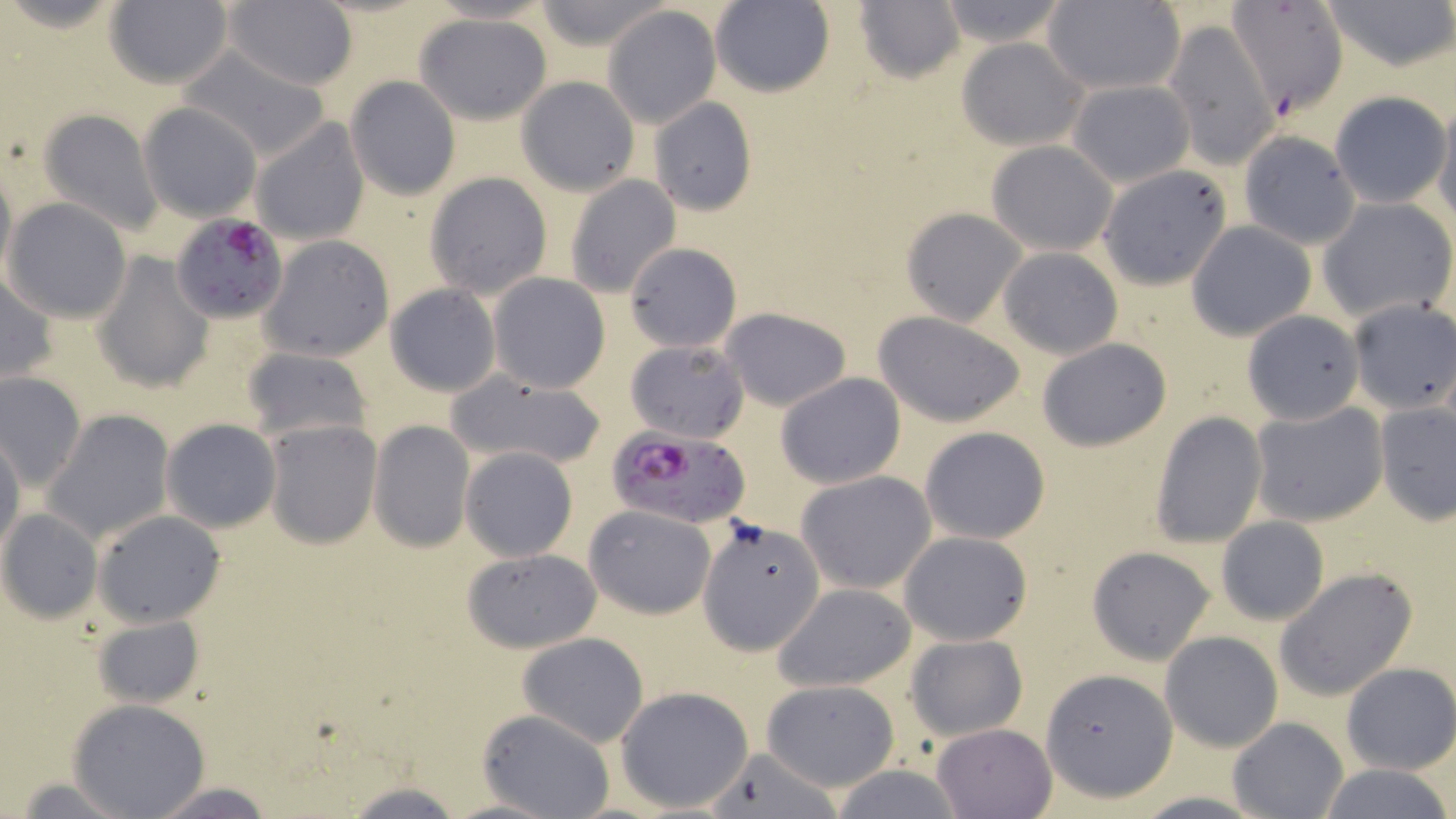
Summary:
  - Coordinate format: approximate bounding boxes as (x1,y1)-(x2,y2) corner pairs in pixels
  - Plasmodium falciparum-infected red blood cell locations: (171,212)-(290,325), (612,425)-(747,527)
  - Uninfected red blood cell locations: (105,0)-(233,89), (221,0)-(358,90), (530,0)-(674,50), (934,0)-(1071,48), (1316,0)-(1456,75), (710,1)-(836,97), (852,1)-(967,84), (1224,1)-(1350,115), (1043,2)-(1185,94), (603,7)-(720,128), (414,13)-(553,123), (1162,19)-(1278,170), (956,37)-(1087,151), (179,48)-(332,161), (345,76)-(460,201), (515,77)-(639,197), (1067,79)-(1195,187), (1330,92)-(1450,208), (648,96)-(757,215), (1432,97)-(1456,227), (138,102)-(264,221), (38,108)-(162,233), (250,116)-(371,246), (1236,130)-(1361,248), (986,139)-(1119,255), (0,162)-(16,291), (1100,164)-(1232,287), (425,172)-(554,299), (563,175)-(681,300), (4,197)-(133,323), (1318,197)-(1455,321), (902,207)-(1026,326), (1187,221)-(1316,340), (259,235)-(395,363), (625,242)-(743,352), (998,246)-(1123,359), (93,251)-(214,392), (1,273)-(58,384), (488,273)-(610,393), (385,282)-(501,397), (1346,300)-(1456,414), (720,307)-(852,410), (1243,309)-(1364,427), (871,310)-(1028,426), (1036,338)-(1173,451), (624,339)-(750,444), (241,347)-(372,443), (446,370)-(608,470), (0,371)-(86,489), (777,372)-(905,489), (1248,399)-(1389,527), (1374,401)-(1456,525), (42,409)-(175,546), (1151,414)-(1268,547), (162,418)-(281,534), (263,419)-(382,549), (368,420)-(475,552), (920,426)-(1050,544), (0,434)-(24,558), (460,447)-(578,561), (796,471)-(935,595), (584,503)-(717,618), (0,509)-(103,623), (94,510)-(227,628), (1215,516)-(1329,626), (699,518)-(826,655), (899,531)-(1032,644), (1087,545)-(1215,665), (461,548)-(603,653), (1274,567)-(1419,703), (771,581)-(918,692), (91,615)-(205,708), (1160,631)-(1283,751), (517,632)-(650,747), (905,634)-(1027,740), (1341,663)-(1456,776), (1041,669)-(1178,801), (759,680)-(900,791), (615,685)-(755,814), (67,698)-(212,819), (476,708)-(618,819), (1227,717)-(1347,819), (931,723)-(1056,818), (702,745)-(844,819), (1313,763)-(1456,819), (7,774)-(143,817), (339,779)-(468,818), (147,781)-(279,818)
  - Slide-level diagnosis: Plasmodium falciparum
  - Stain: May-Grünwald-Giemsa
  - Magnification: 1000x
  - Modality: optical microscopy
  - Preparation: thin blood smear
  - Field of view: one of a larger specimen
  - Image size: 1456×819 pixels